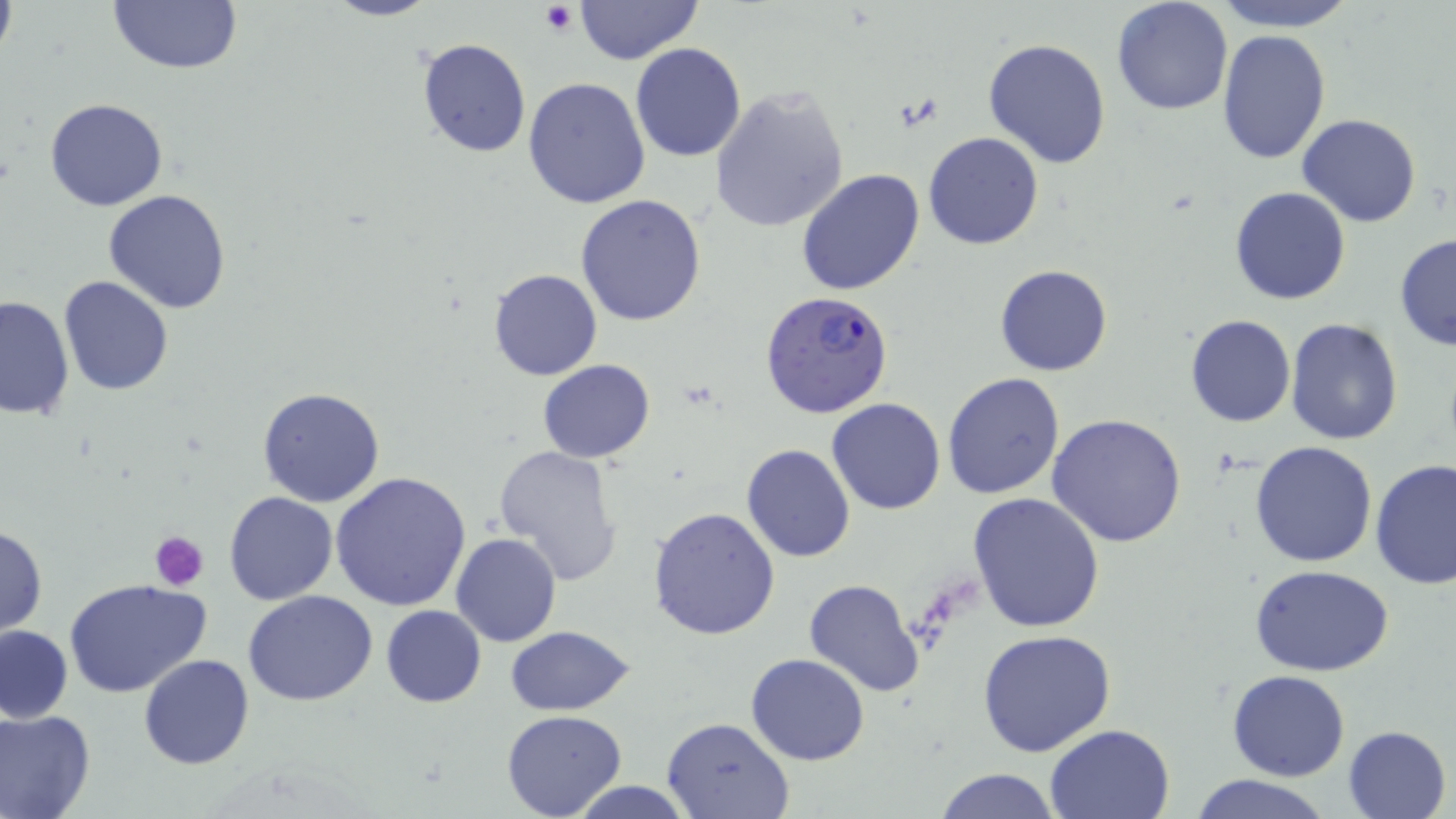

slide-level diagnosis = Plasmodium falciparum
modality = light microscopy
field of view = one of a larger specimen
preparation = thin blood film
uninfected red blood cell locations = approximate bounding boxes as [x1, y1, x2, y2] in pixels: [105, 0, 243, 77], [319, 0, 441, 22], [576, 0, 702, 65], [1111, 0, 1234, 116], [1209, 0, 1360, 32], [0, 2, 16, 59], [1215, 29, 1332, 164], [415, 36, 532, 159], [983, 38, 1112, 169], [629, 43, 747, 163], [542, 65, 739, 190], [523, 77, 652, 210], [709, 87, 850, 233], [44, 97, 168, 212], [1296, 114, 1422, 227], [923, 131, 1045, 251], [796, 169, 925, 297], [1230, 185, 1351, 306], [105, 190, 233, 312], [576, 194, 707, 325], [1393, 233, 1455, 351], [994, 264, 1111, 377], [488, 268, 602, 381], [59, 275, 174, 395], [0, 295, 74, 420], [1185, 314, 1296, 427], [1284, 317, 1403, 446], [538, 359, 656, 463], [942, 371, 1067, 501], [256, 387, 385, 507], [827, 397, 945, 514], [1046, 413, 1187, 548], [1249, 440, 1379, 568], [740, 444, 856, 563], [493, 445, 625, 587], [1369, 459, 1455, 590], [332, 473, 472, 613], [224, 490, 338, 605], [969, 490, 1105, 633], [647, 506, 781, 642], [0, 523, 47, 637], [450, 533, 561, 647], [1252, 566, 1392, 678], [64, 578, 212, 699], [804, 578, 923, 696], [243, 589, 378, 707], [380, 604, 486, 708], [0, 625, 73, 723], [505, 625, 635, 715], [975, 630, 1119, 758], [746, 653, 871, 766], [138, 654, 254, 769], [1227, 670, 1349, 782], [0, 707, 96, 819], [502, 710, 628, 819], [662, 716, 795, 819], [1045, 723, 1175, 818], [1343, 725, 1452, 818], [932, 767, 1059, 819], [1188, 773, 1332, 819], [565, 780, 699, 817]
magnification = 1000x
Plasmodium falciparum-infected red blood cell locations = approximate bounding boxes as [x1, y1, x2, y2] in pixels: [758, 289, 895, 419]
stain = May-Grünwald-Giemsa
image size = 1456×819 pixels
platelet locations = approximate bounding boxes as [x1, y1, x2, y2] in pixels: [540, 3, 578, 34], [150, 530, 209, 590]